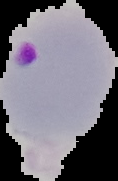
Cell region segmented out of the field of view; the surrounding area is masked to black. From a thin blood smear. Result: Plasmodium parasites identified. Image is 118×181 pixels.